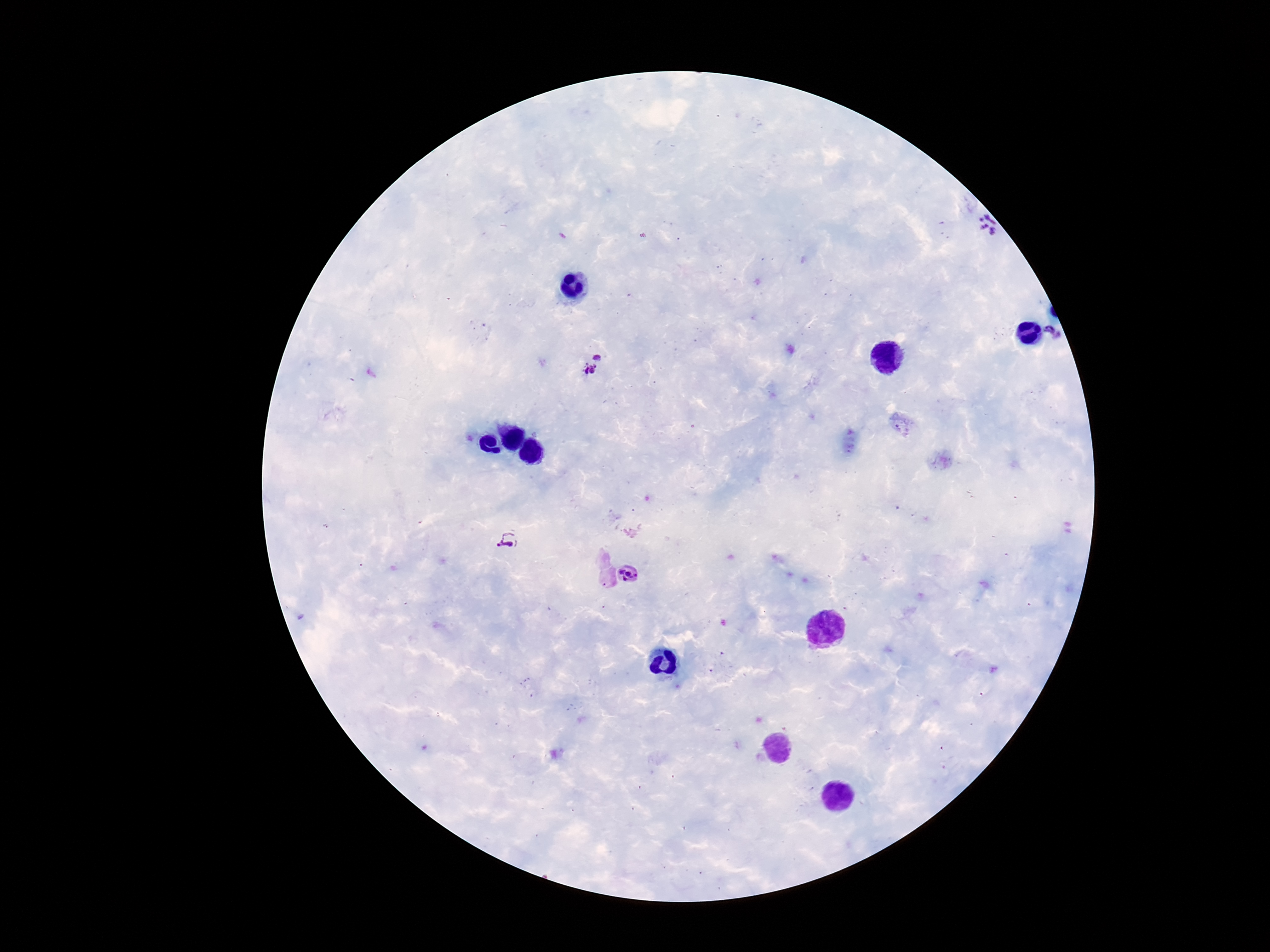
Approximate centers as [x, y] in pixels.
Summary:
  - Plasmodium parasite locations: [983, 228], [1054, 332], [593, 364], [508, 541], [633, 573]
  - Preparation: thick peripheral-blood smear
  - Patient malaria status: infected
  - Stain: Giemsa
  - Field of view: single
  - Magnification: 100x
  - Image size: 1270×952 pixels
  - Capture: smartphone camera through the microscope eyepiece